Describe the morphology of the erythrocytes.
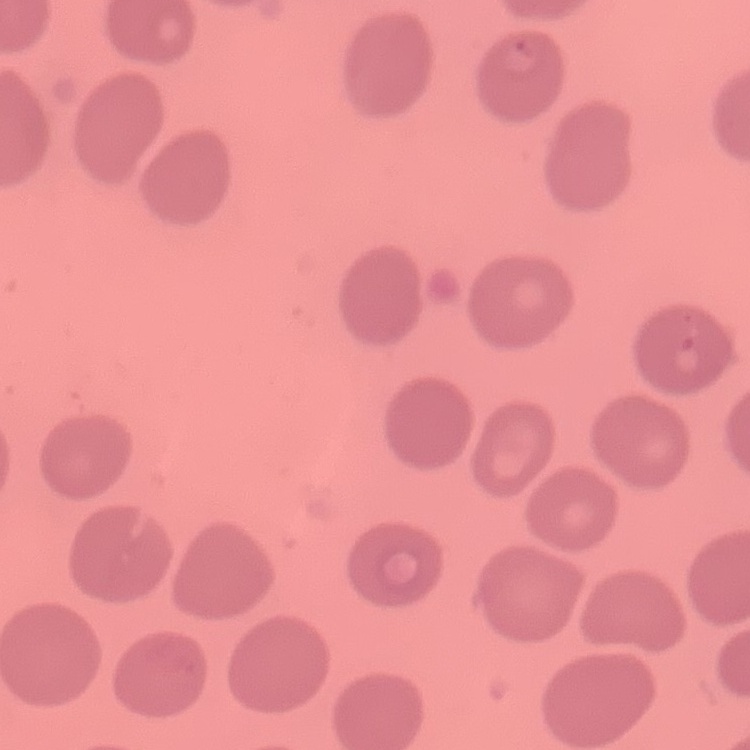

No rouleaux formation.

{
  "preparation": "thin blood film",
  "image_type": "square crop of a larger photomicrograph",
  "stain": "Field's or Giemsa"
}